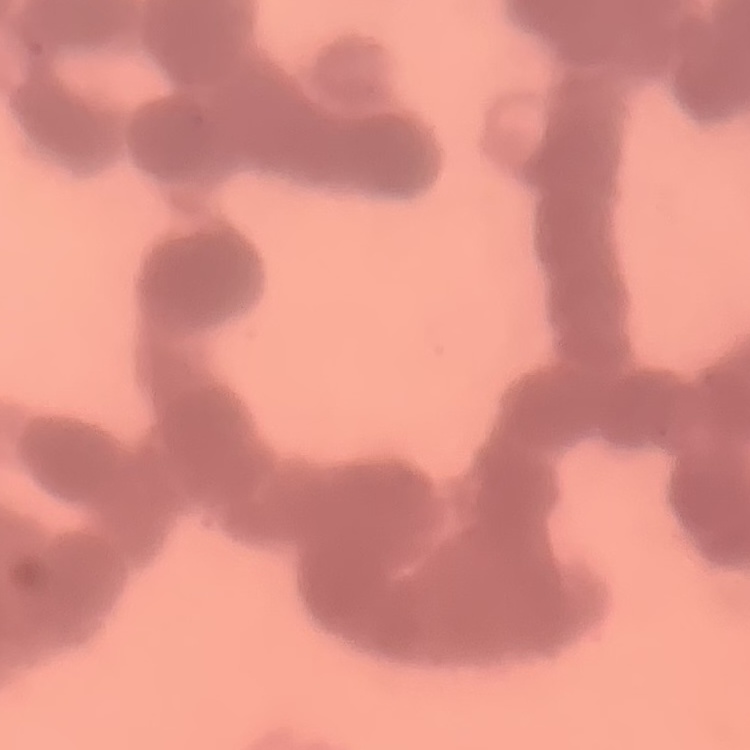

The erythrocytes show rouleaux formation. Stained with either Field's or Giemsa. One tile cut from a larger photomicrograph. Thin blood film.